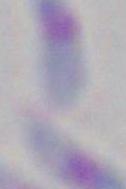

Summary:
  - Identification: Toxoplasma gondii
  - Magnification: 1000x
  - Modality: micrograph